Locate and identify every blood parasite.
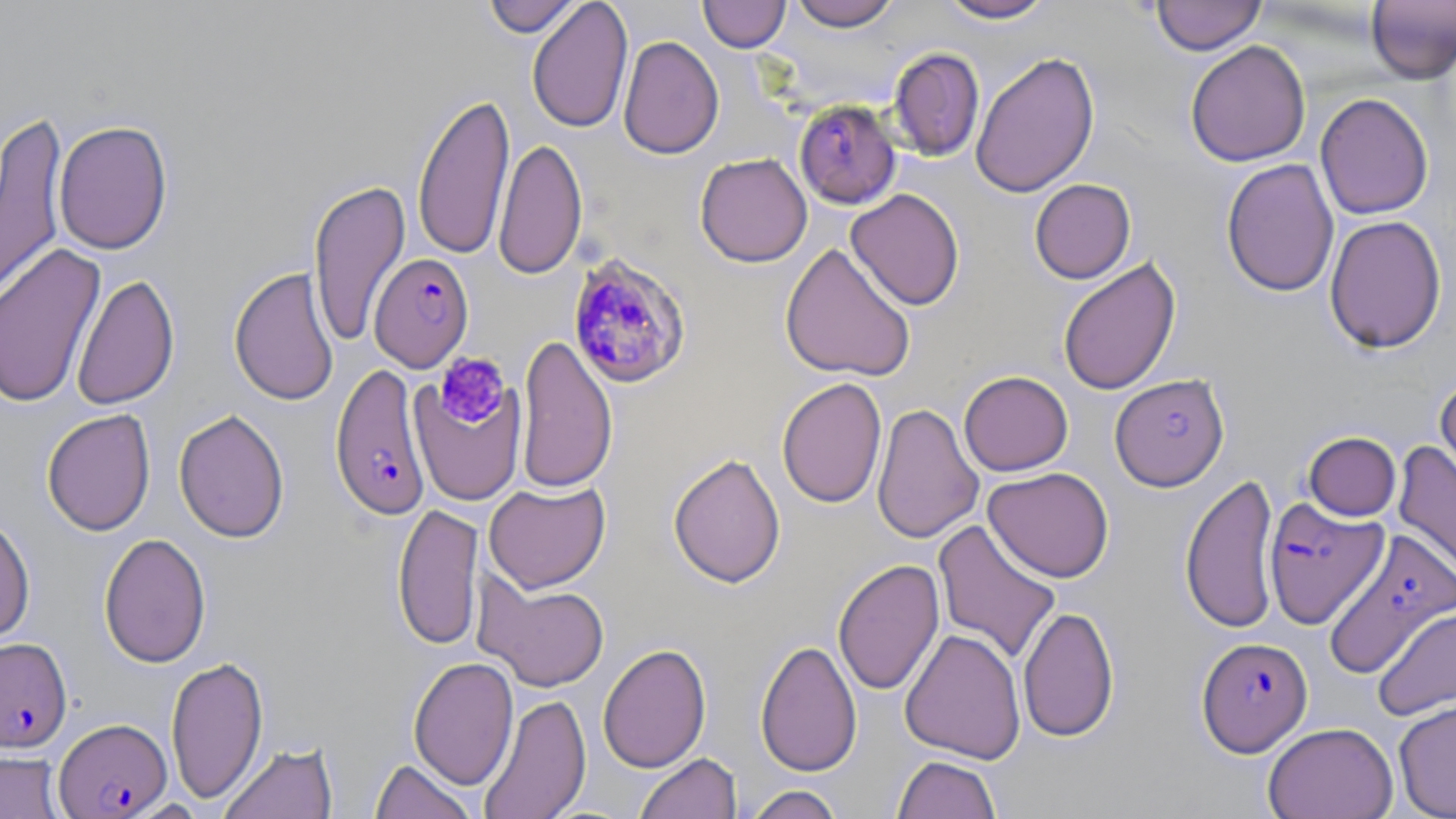
Approximate bounding boxes as [x1, y1, x2, y2] in pixels.
Plasmodium falciparum-infected red blood cells: [794, 99, 902, 209], [369, 253, 474, 372], [566, 253, 693, 390], [330, 362, 429, 521], [1109, 373, 1230, 491], [1264, 498, 1388, 629], [1323, 528, 1456, 679], [0, 637, 72, 752], [1196, 637, 1312, 757], [54, 717, 172, 818].
No Plasmodium ovale, Plasmodium malariae, Plasmodium vivax, Babesia divergens, or Trypanosoma brucei observed.

Summary:
  - Uninfected red blood cell locations: [482, 0, 582, 37], [527, 0, 633, 134], [699, 0, 790, 52], [788, 0, 901, 31], [937, 0, 1056, 24], [1151, 0, 1266, 55], [1365, 0, 1456, 83], [617, 35, 724, 159], [1185, 39, 1311, 167], [888, 47, 985, 162], [970, 50, 1100, 198], [412, 90, 514, 260], [1315, 92, 1434, 220], [0, 109, 68, 309], [53, 119, 173, 255], [493, 137, 587, 281], [695, 153, 812, 267], [1221, 158, 1339, 298], [308, 177, 411, 346], [1029, 178, 1136, 284], [846, 188, 965, 310], [1324, 215, 1447, 354], [0, 242, 106, 409], [780, 242, 916, 382], [1057, 257, 1181, 396], [229, 267, 339, 406], [71, 274, 179, 411], [516, 334, 617, 494], [959, 370, 1073, 476], [408, 376, 527, 508], [1435, 376, 1456, 499], [776, 377, 887, 508], [871, 402, 984, 544], [42, 408, 156, 536], [173, 409, 290, 543], [1301, 430, 1404, 522], [1393, 441, 1456, 588], [668, 451, 786, 589], [984, 467, 1115, 582], [1180, 473, 1280, 635], [484, 481, 611, 593], [392, 502, 484, 650], [0, 514, 36, 645], [932, 519, 1062, 665], [98, 532, 211, 668], [833, 558, 945, 697], [474, 573, 611, 692], [1018, 605, 1119, 743], [1372, 606, 1456, 723], [900, 627, 1026, 765], [755, 639, 862, 776], [597, 643, 711, 773], [165, 655, 269, 804], [408, 656, 519, 791], [478, 693, 591, 819], [1393, 698, 1456, 819], [1262, 722, 1398, 819], [219, 742, 338, 819], [0, 750, 68, 819], [634, 753, 741, 819], [892, 755, 1001, 819], [370, 757, 477, 819], [742, 784, 845, 819]
  - Platelet locations: [434, 352, 511, 429]
  - Slide-level diagnosis: Plasmodium falciparum
  - Preparation: thin blood smear
  - Stain: May-Grünwald-Giemsa
  - Magnification: 1000x
  - Image size: 1456×819 pixels
  - Modality: light microscopy
  - Field of view: one of a larger specimen